Assess this cell for malaria.
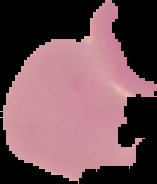

It is uninfected.

Summary:
  - Image size: 157×184 pixels
  - Preparation: thin blood smear
  - Image type: segmented cell region on a black background